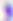
Summary:
  - Identification: Toxoplasma gondii
  - Modality: micrograph
  - Magnification: 400x